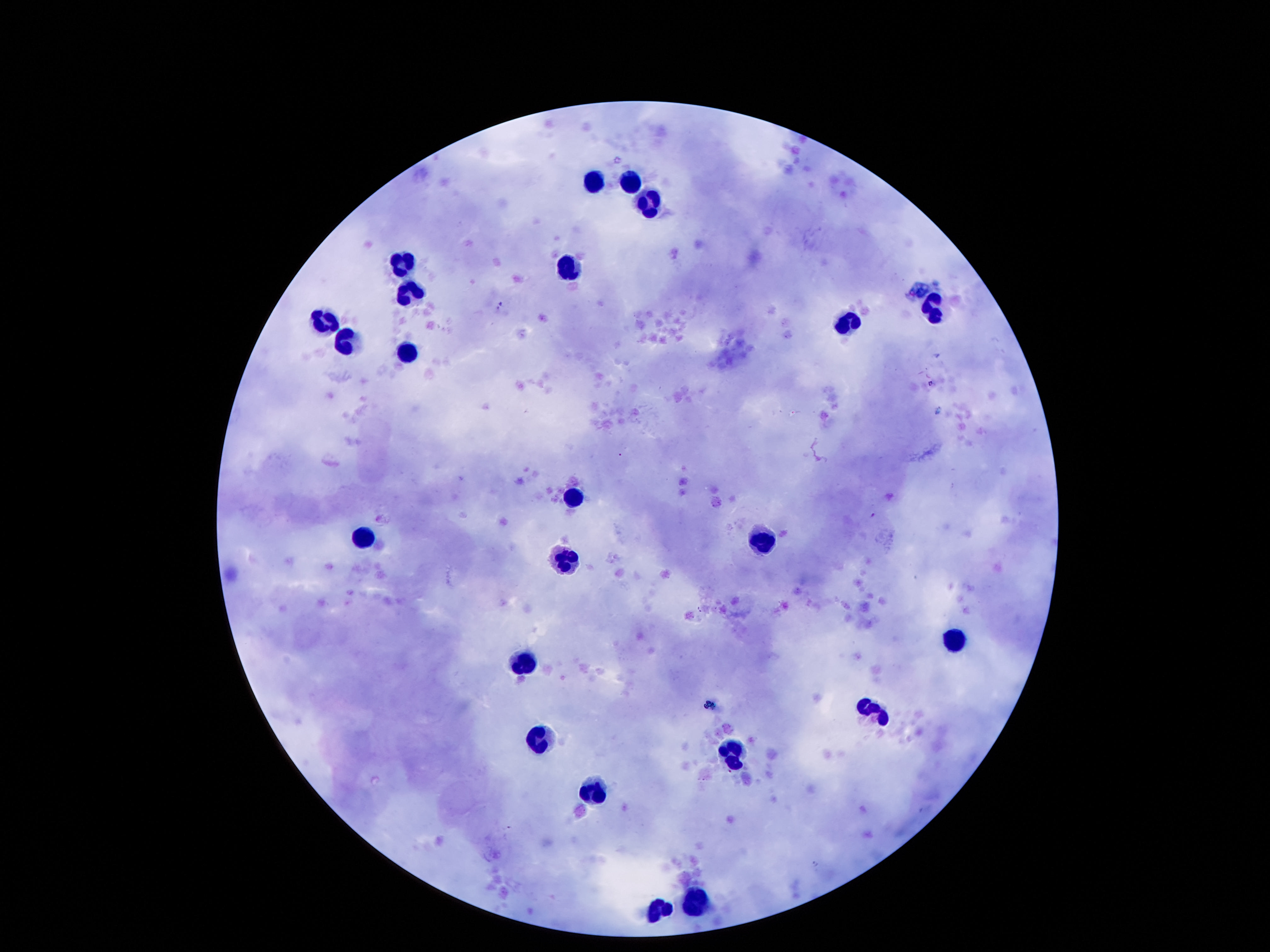 Approximate centers as [x, y] in pixels. Leukocyte locations: [591, 179], [632, 179], [650, 201], [406, 259], [564, 269], [411, 289], [935, 304], [322, 318], [845, 322], [345, 341], [408, 351], [572, 498], [361, 537], [763, 541], [560, 560], [954, 634], [521, 658], [878, 709], [540, 736], [730, 750], [595, 787], [695, 902], [658, 910]. Smartphone photograph taken through the microscope eyepiece. One field from this slide. Giemsa stain. Thick blood film. 100x magnification. Image is 1270×952 pixels. Patient malaria status: negative.